State the preparation type.
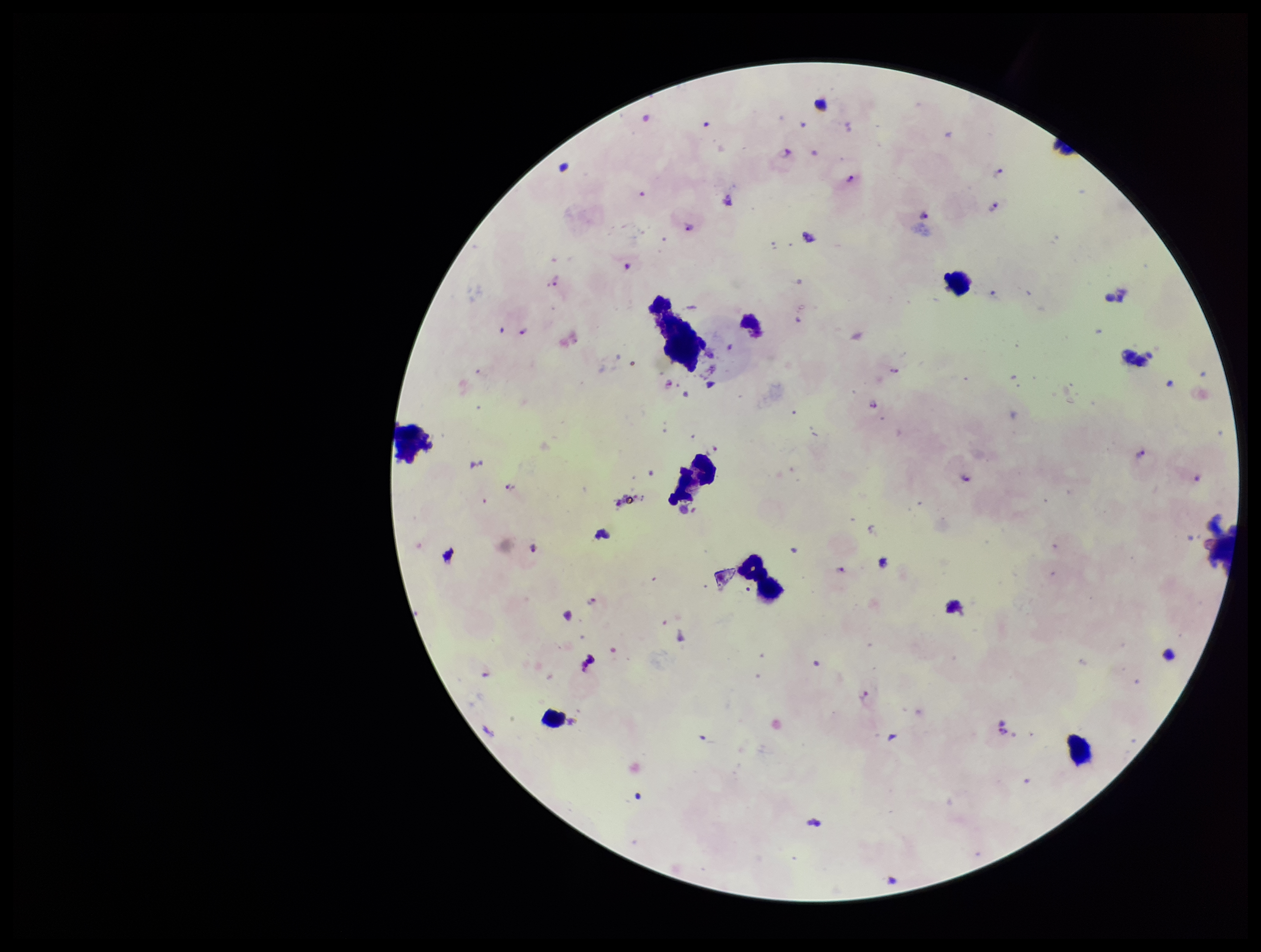

A thick smear.

Patient malaria status: positive. Smartphone photograph taken through the eyepiece of a microscope. Species reported for this patient: Plasmodium falciparum. Leukocyte count: 5. Plasmodium parasites: identified. One field from this slide. Image is 1261×952 pixels. Parasite count: 30. Stained with Giemsa.